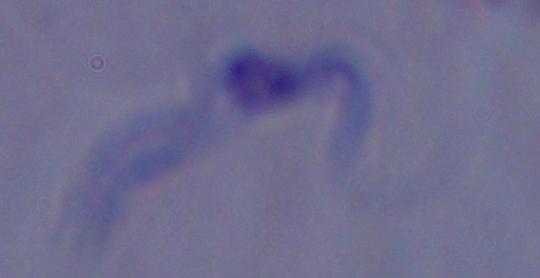 A trypanosome is seen. 1000x magnification. Micrograph.